Evaluate for Plasmodium parasites.
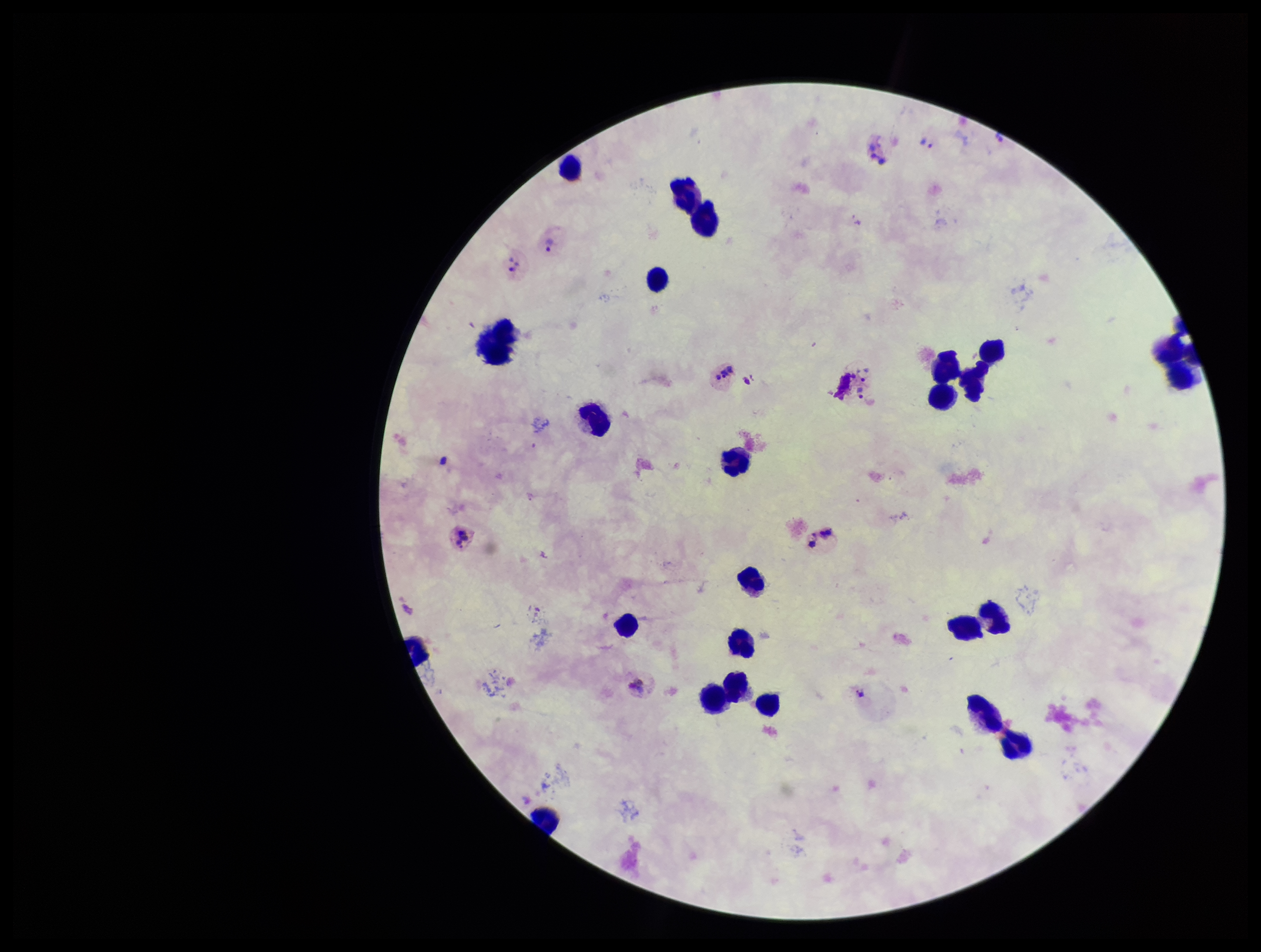
Identified.

Smartphone photograph taken through the eyepiece of a microscope. Giemsa stain. One field from this slide. Species reported for this patient: Plasmodium vivax. Patient malaria status: positive. Image is 1261×952 pixels. Preparation: thick blood smear. Parasite count: 5. Leukocyte count: 22.